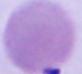 Micrograph. A red blood cell is seen. 1000x magnification.